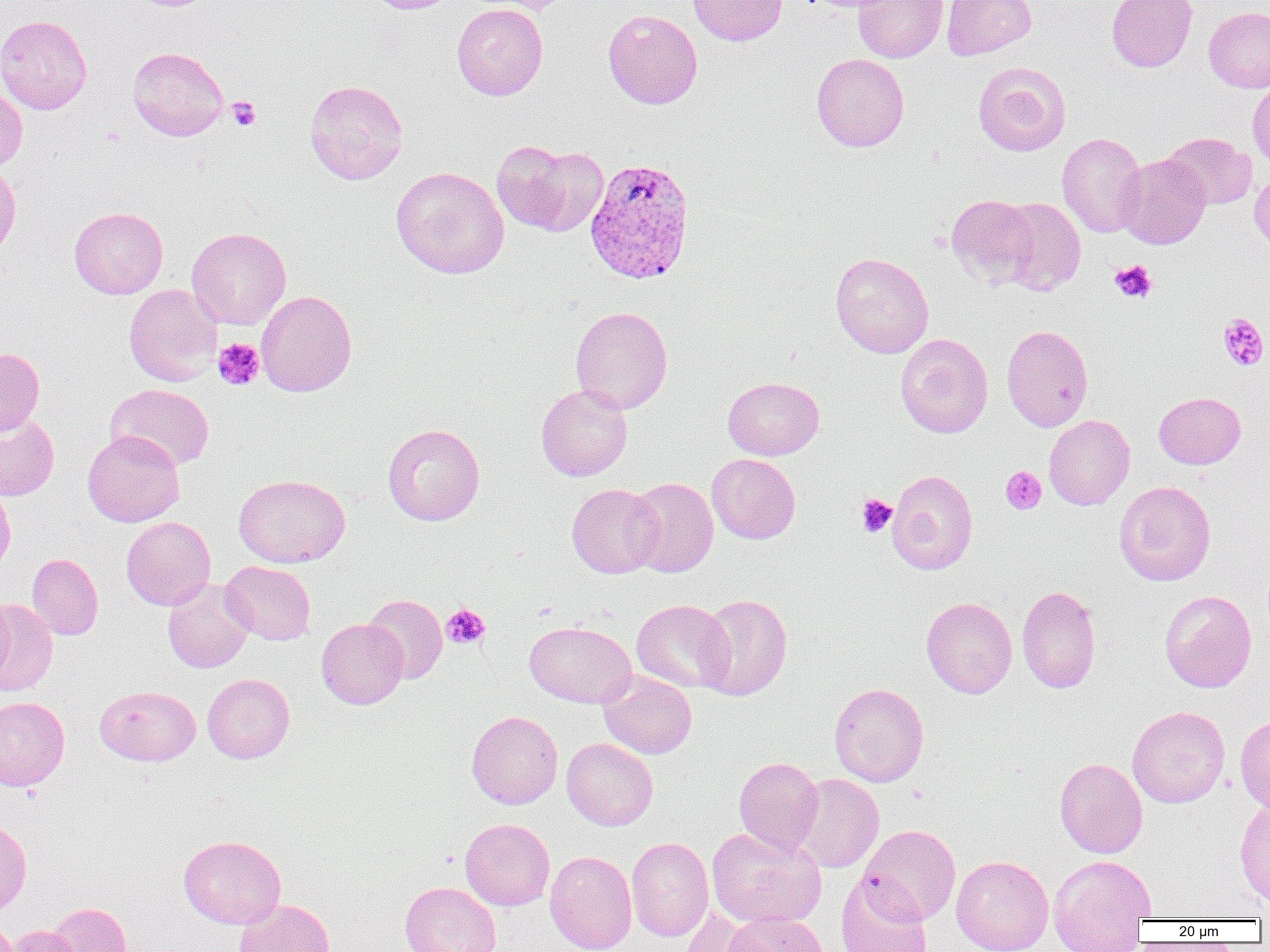 Approximate bounding boxes as named x1/y1/x2/y2 corners in pixels. Platelet locations: (x1=226, y1=96, x2=260, y2=131), (x1=1110, y1=260, x2=1157, y2=304), (x1=1217, y1=312, x2=1269, y2=371), (x1=213, y1=338, x2=265, y2=390), (x1=1001, y1=466, x2=1046, y2=514), (x1=857, y1=494, x2=897, y2=537), (x1=441, y1=604, x2=490, y2=649). Plasmodium vivax-infected red blood cell locations: (x1=584, y1=156, x2=696, y2=284). Uninfected red blood cell locations: (x1=363, y1=0, x2=460, y2=14), (x1=465, y1=0, x2=576, y2=14), (x1=687, y1=0, x2=787, y2=46), (x1=853, y1=0, x2=948, y2=63), (x1=942, y1=0, x2=1036, y2=60), (x1=1106, y1=0, x2=1197, y2=72), (x1=452, y1=3, x2=548, y2=100), (x1=1203, y1=6, x2=1270, y2=93), (x1=603, y1=9, x2=703, y2=109), (x1=0, y1=14, x2=92, y2=114), (x1=127, y1=46, x2=228, y2=141), (x1=812, y1=53, x2=909, y2=152), (x1=973, y1=61, x2=1071, y2=156), (x1=305, y1=79, x2=407, y2=185), (x1=1247, y1=79, x2=1270, y2=173), (x1=0, y1=81, x2=27, y2=171), (x1=1057, y1=132, x2=1147, y2=238), (x1=1162, y1=132, x2=1256, y2=210), (x1=492, y1=140, x2=577, y2=234), (x1=523, y1=146, x2=609, y2=236), (x1=1117, y1=154, x2=1210, y2=249), (x1=0, y1=161, x2=21, y2=260), (x1=391, y1=166, x2=509, y2=279), (x1=1250, y1=169, x2=1270, y2=252), (x1=946, y1=194, x2=1040, y2=288), (x1=995, y1=197, x2=1086, y2=295), (x1=69, y1=207, x2=168, y2=299), (x1=186, y1=227, x2=291, y2=329), (x1=830, y1=252, x2=934, y2=358), (x1=123, y1=284, x2=222, y2=386), (x1=256, y1=290, x2=357, y2=396), (x1=570, y1=305, x2=672, y2=414), (x1=1001, y1=325, x2=1093, y2=432), (x1=895, y1=333, x2=993, y2=438), (x1=0, y1=347, x2=45, y2=435), (x1=723, y1=376, x2=824, y2=460), (x1=105, y1=384, x2=214, y2=471), (x1=536, y1=384, x2=632, y2=481), (x1=1154, y1=392, x2=1246, y2=469), (x1=0, y1=412, x2=59, y2=500), (x1=1044, y1=415, x2=1135, y2=510), (x1=382, y1=424, x2=484, y2=526), (x1=82, y1=430, x2=185, y2=527), (x1=707, y1=454, x2=801, y2=544), (x1=887, y1=469, x2=978, y2=575), (x1=234, y1=474, x2=350, y2=568), (x1=626, y1=477, x2=718, y2=577), (x1=0, y1=478, x2=16, y2=576), (x1=1114, y1=481, x2=1216, y2=585), (x1=566, y1=483, x2=663, y2=578), (x1=121, y1=517, x2=216, y2=610), (x1=26, y1=553, x2=103, y2=640), (x1=220, y1=560, x2=316, y2=645), (x1=162, y1=578, x2=255, y2=673), (x1=1017, y1=584, x2=1102, y2=694), (x1=1159, y1=590, x2=1257, y2=692), (x1=696, y1=593, x2=792, y2=701), (x1=363, y1=594, x2=447, y2=684), (x1=0, y1=596, x2=15, y2=687), (x1=921, y1=597, x2=1017, y2=698), (x1=631, y1=599, x2=734, y2=693), (x1=0, y1=600, x2=58, y2=695), (x1=316, y1=618, x2=408, y2=709), (x1=525, y1=621, x2=637, y2=707), (x1=599, y1=671, x2=697, y2=759), (x1=202, y1=673, x2=295, y2=763), (x1=829, y1=683, x2=929, y2=787), (x1=94, y1=685, x2=201, y2=766), (x1=0, y1=697, x2=70, y2=791), (x1=1127, y1=706, x2=1229, y2=808), (x1=466, y1=710, x2=563, y2=809), (x1=1235, y1=713, x2=1270, y2=816), (x1=561, y1=738, x2=658, y2=830), (x1=734, y1=756, x2=823, y2=856), (x1=1054, y1=758, x2=1147, y2=858), (x1=790, y1=773, x2=884, y2=873), (x1=1234, y1=799, x2=1270, y2=909), (x1=0, y1=818, x2=31, y2=915), (x1=460, y1=818, x2=554, y2=911), (x1=859, y1=825, x2=961, y2=924), (x1=707, y1=826, x2=826, y2=929), (x1=178, y1=835, x2=286, y2=929), (x1=626, y1=837, x2=713, y2=942), (x1=545, y1=850, x2=637, y2=952), (x1=1048, y1=854, x2=1156, y2=952), (x1=951, y1=855, x2=1054, y2=952), (x1=836, y1=873, x2=932, y2=952), (x1=400, y1=881, x2=501, y2=952), (x1=235, y1=898, x2=336, y2=952), (x1=45, y1=902, x2=133, y2=952), (x1=680, y1=906, x2=763, y2=952), (x1=722, y1=912, x2=829, y2=952), (x1=0, y1=916, x2=19, y2=952), (x1=6, y1=925, x2=84, y2=952). Slide-level diagnosis: Plasmodium vivax. Image is 1270×952 pixels. Single field of view. Light microscopy. 1000x magnification. Thin blood smear.